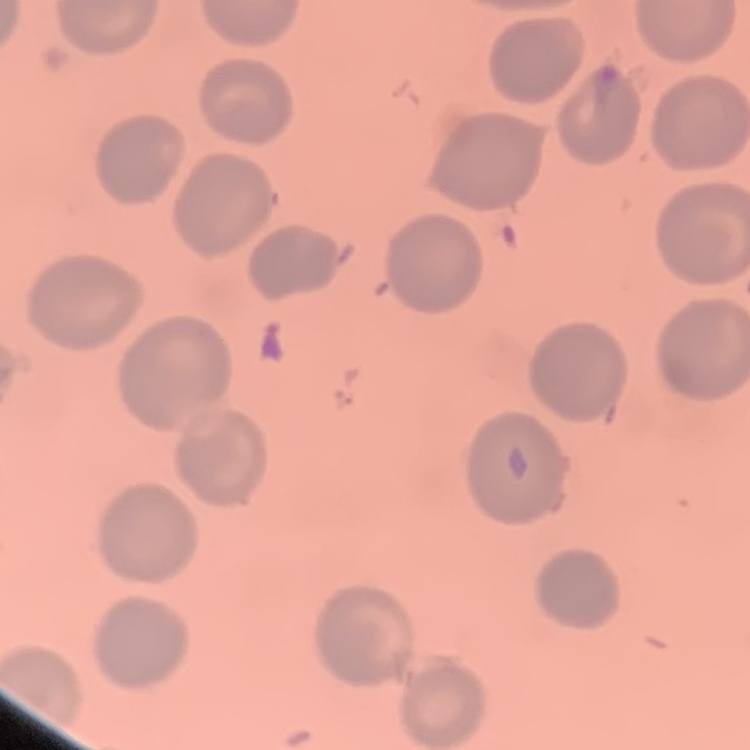
Summary:
  - Red blood cell morphology: no rouleaux formation
  - Image type: one tile cut from a larger photomicrograph
  - Preparation: thin blood smear
  - Stain: Field's or Giemsa